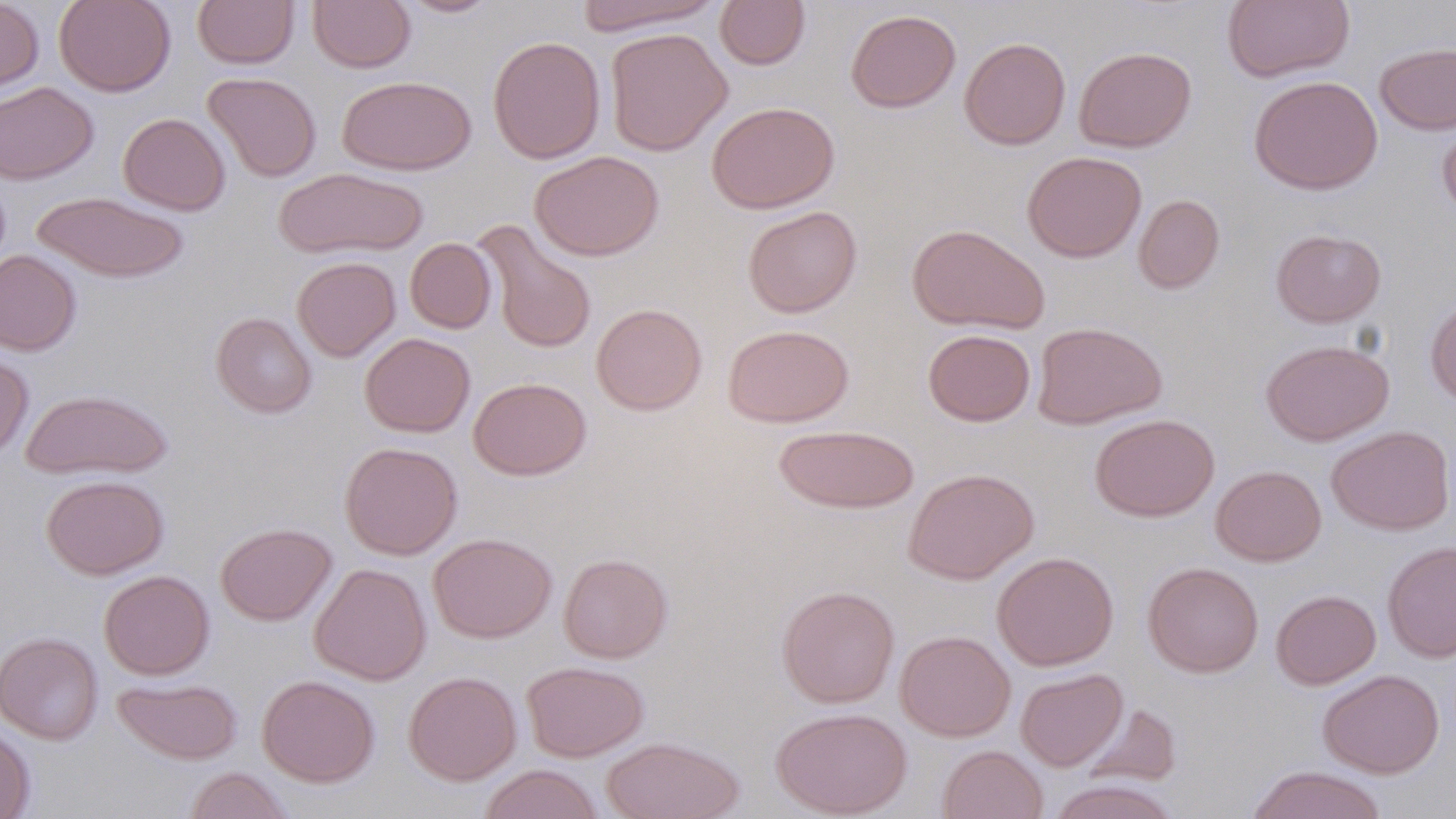

Approximate bounding boxes as (x1, y1, x2, y2) in pixels. Uninfected red blood cell locations: (0, 0, 43, 94), (53, 0, 176, 97), (193, 0, 299, 69), (308, 0, 416, 73), (395, 0, 502, 18), (572, 0, 723, 36), (714, 0, 810, 70), (1221, 0, 1355, 83), (846, 9, 961, 113), (605, 27, 733, 156), (487, 35, 605, 164), (959, 37, 1071, 150), (1374, 42, 1456, 135), (1074, 46, 1196, 152), (203, 72, 321, 182), (337, 74, 476, 176), (1248, 75, 1383, 195), (0, 82, 98, 185), (707, 101, 840, 214), (1436, 111, 1456, 224), (118, 112, 231, 216), (530, 150, 665, 261), (1022, 151, 1146, 262), (274, 167, 427, 259), (31, 192, 191, 283), (1133, 194, 1225, 294), (742, 205, 862, 318), (474, 220, 597, 354), (906, 223, 1050, 335), (1271, 228, 1386, 327), (405, 238, 496, 333), (0, 250, 82, 355), (291, 256, 401, 362), (1425, 298, 1456, 407), (591, 303, 707, 416), (211, 312, 317, 418), (1031, 322, 1167, 430), (723, 324, 854, 428), (923, 329, 1035, 426), (359, 333, 474, 437), (1260, 339, 1394, 446), (0, 349, 34, 461), (468, 377, 591, 480), (20, 390, 173, 480), (1090, 413, 1219, 522), (773, 424, 920, 514), (1326, 425, 1455, 535), (339, 441, 462, 559), (1210, 464, 1326, 566), (903, 467, 1039, 585), (40, 475, 169, 579), (215, 522, 336, 626), (429, 532, 557, 643), (1382, 541, 1456, 663), (992, 551, 1119, 671), (558, 553, 673, 663), (1142, 561, 1264, 677), (309, 563, 432, 685), (99, 570, 214, 679), (776, 585, 899, 708), (1270, 589, 1381, 689), (895, 630, 1015, 742), (0, 632, 103, 744), (521, 660, 649, 762), (1016, 668, 1127, 771), (1318, 669, 1445, 778), (403, 670, 522, 786), (257, 674, 380, 787), (113, 677, 243, 764), (1080, 703, 1181, 788), (771, 706, 912, 818), (0, 722, 35, 818), (601, 736, 744, 819), (937, 744, 1048, 819), (478, 764, 604, 819), (1246, 765, 1389, 819), (183, 767, 294, 819), (1046, 779, 1183, 819). Slide-level diagnosis: negative for blood parasites. May-Grünwald-Giemsa-stained preparation. One field of a larger specimen. Light microscopy. Thin blood film. Captured at 1000x magnification. Image is 1456×819 pixels.